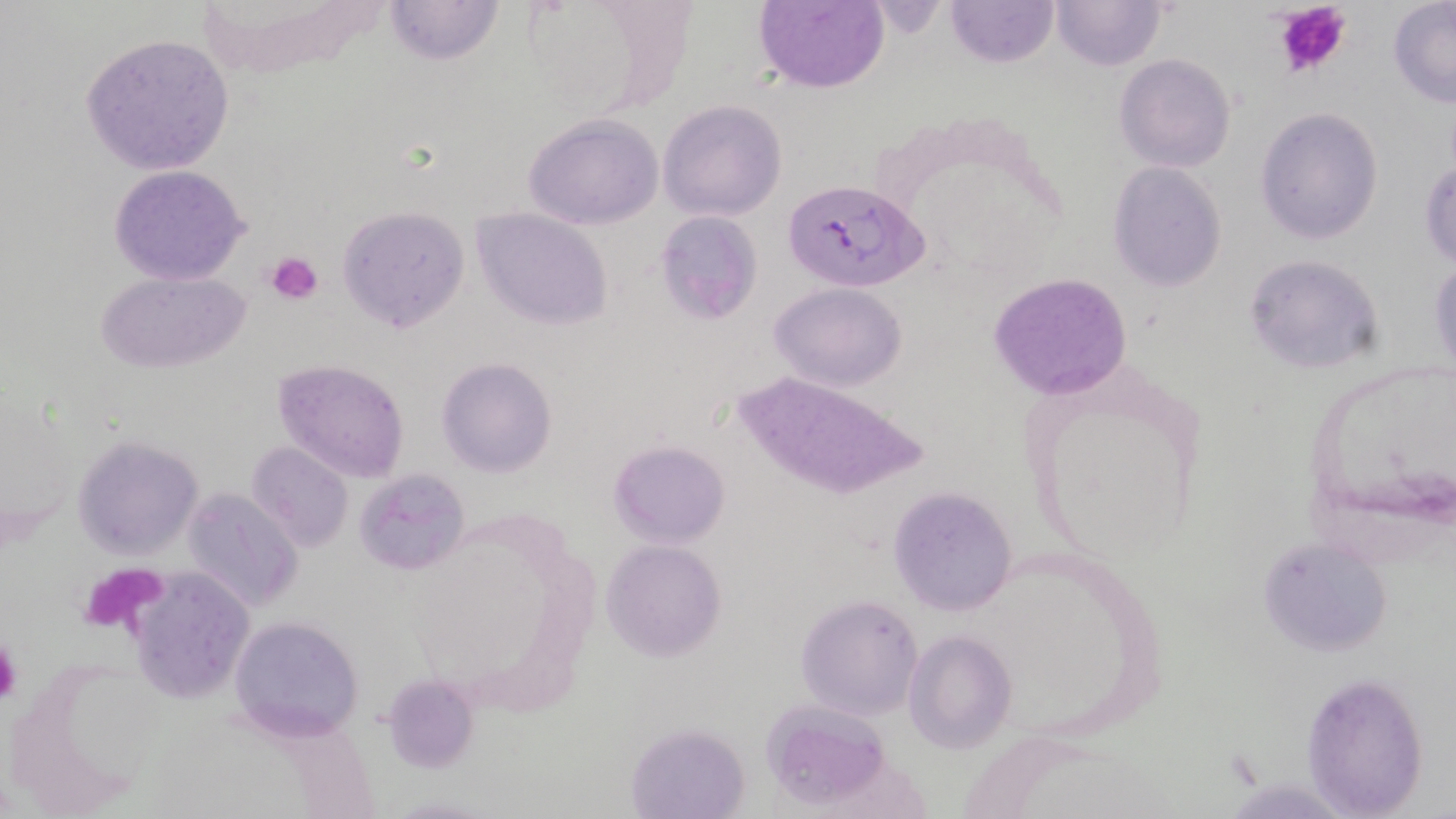
slide-level diagnosis = Plasmodium falciparum
platelet locations = approximate bounding boxes as named x1/y1/x2/y2 corners in pixels: (x1=1273, y1=0, x2=1353, y2=81), (x1=267, y1=249, x2=325, y2=304), (x1=0, y1=635, x2=21, y2=707)
modality = light microscopy
field of view = single
magnification = 1000x
uninfected red blood cell locations = approximate bounding boxes as named x1/y1/x2/y2 corners in pixels: (x1=383, y1=0, x2=505, y2=67), (x1=753, y1=0, x2=889, y2=93), (x1=946, y1=0, x2=1058, y2=68), (x1=1051, y1=0, x2=1167, y2=71), (x1=1388, y1=0, x2=1456, y2=107), (x1=80, y1=33, x2=234, y2=175), (x1=1114, y1=54, x2=1235, y2=172), (x1=658, y1=99, x2=787, y2=221), (x1=1255, y1=107, x2=1384, y2=246), (x1=523, y1=114, x2=664, y2=228), (x1=1421, y1=158, x2=1456, y2=269), (x1=1108, y1=163, x2=1228, y2=291), (x1=107, y1=164, x2=252, y2=285), (x1=338, y1=205, x2=470, y2=333), (x1=472, y1=207, x2=612, y2=329), (x1=655, y1=211, x2=761, y2=323), (x1=1243, y1=252, x2=1386, y2=374), (x1=1427, y1=253, x2=1456, y2=378), (x1=95, y1=269, x2=249, y2=373), (x1=988, y1=271, x2=1136, y2=401), (x1=770, y1=281, x2=908, y2=390), (x1=272, y1=357, x2=409, y2=483), (x1=437, y1=358, x2=557, y2=477), (x1=1017, y1=360, x2=1209, y2=566), (x1=735, y1=372, x2=929, y2=501), (x1=70, y1=435, x2=202, y2=558), (x1=608, y1=439, x2=729, y2=548), (x1=246, y1=442, x2=353, y2=553), (x1=354, y1=469, x2=469, y2=576), (x1=888, y1=486, x2=1018, y2=615), (x1=181, y1=490, x2=302, y2=612), (x1=1259, y1=536, x2=1395, y2=659), (x1=600, y1=539, x2=727, y2=662), (x1=123, y1=570, x2=257, y2=704), (x1=797, y1=594, x2=923, y2=720), (x1=228, y1=614, x2=366, y2=741), (x1=904, y1=630, x2=1016, y2=752), (x1=1305, y1=674, x2=1430, y2=814), (x1=380, y1=675, x2=477, y2=773), (x1=761, y1=701, x2=891, y2=808), (x1=625, y1=721, x2=750, y2=819)
Plasmodium falciparum-infected red blood cell locations = approximate bounding boxes as named x1/y1/x2/y2 corners in pixels: (x1=784, y1=179, x2=926, y2=292)
preparation = thin blood film
image size = 1456×819 pixels
stain = May-Grünwald-Giemsa